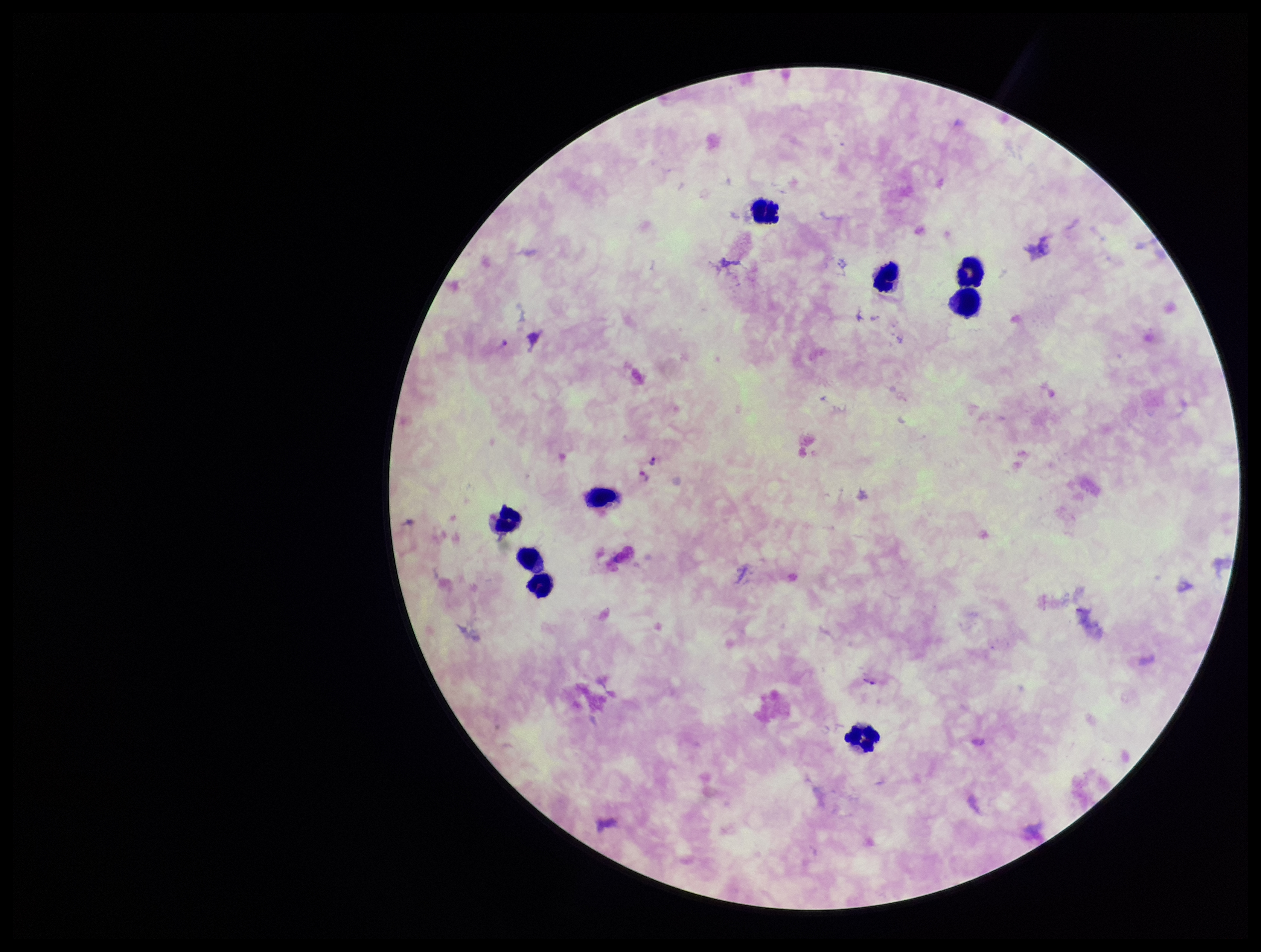
Summary:
  - Leukocyte count: 9
  - Plasmodium parasites: seen
  - Parasite count: 4
  - Capture: smartphone photograph through the microscope eyepiece
  - Patient malaria status: infected
  - Stain: Giemsa
  - Species reported for this patient: Plasmodium falciparum
  - Preparation: thick blood smear
  - Image size: 1261×952 pixels
  - Field of view: single